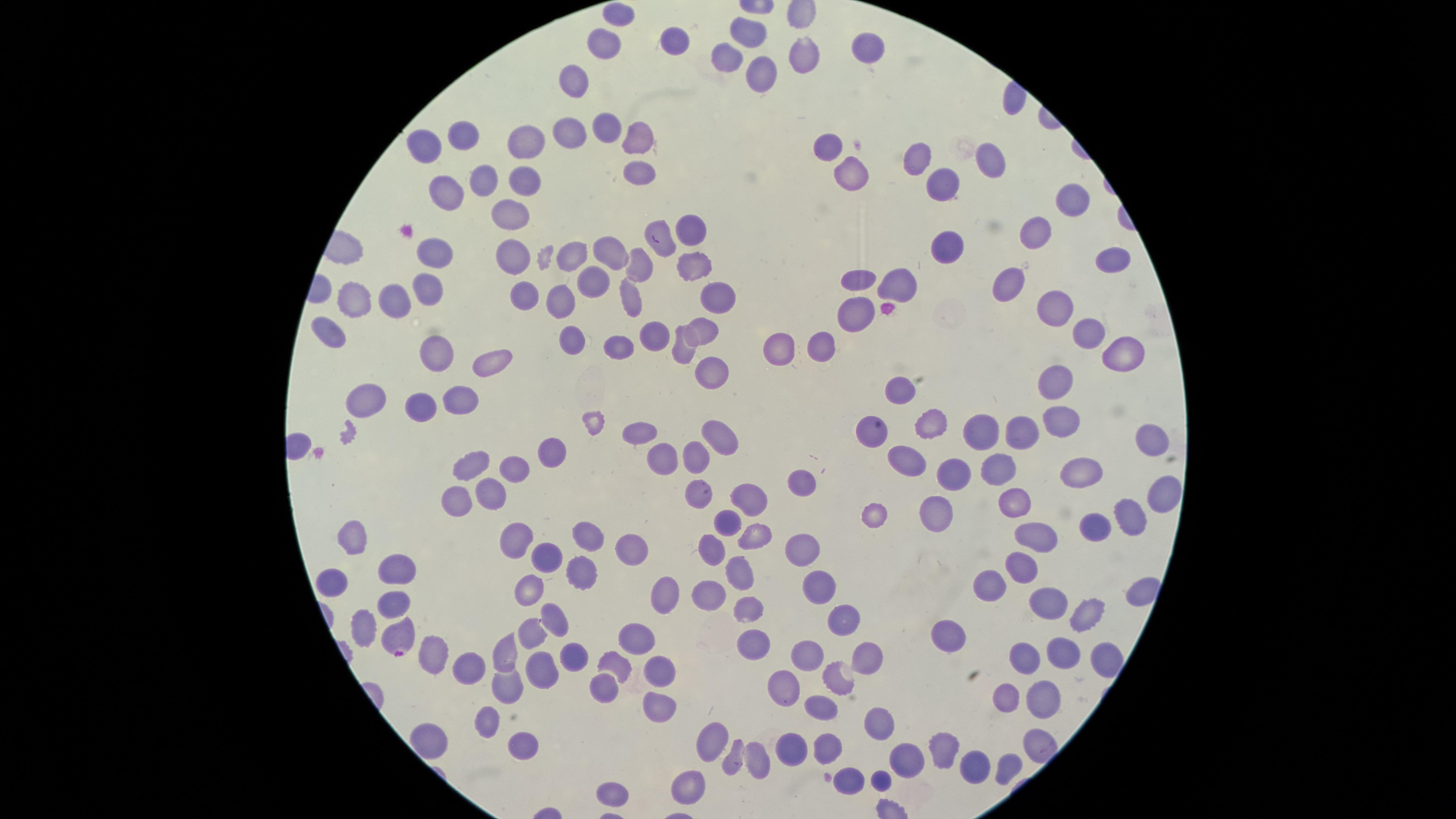

Approximate marker points as [x, y] in pixels.
Summary:
  - Parasitized red blood cells: [403, 639]
  - Uninfected red blood cells: [626, 18], [757, 31], [678, 38], [605, 46], [867, 46], [807, 52], [728, 60], [578, 75], [757, 83], [604, 126], [571, 132], [638, 134], [464, 138], [531, 138], [828, 144], [424, 153], [917, 157], [996, 165], [851, 171], [636, 173], [480, 180], [525, 185], [939, 190], [447, 194], [1076, 200], [510, 213], [690, 226], [659, 228], [1031, 236], [956, 247], [434, 253], [607, 254], [1111, 254], [517, 256], [574, 257], [689, 259], [640, 262], [1013, 279], [859, 280], [899, 284], [595, 286], [430, 288], [717, 291], [531, 294], [631, 298], [355, 299], [398, 299], [1056, 301], [563, 303], [854, 317], [701, 324], [654, 332], [1088, 334], [333, 337], [578, 339], [624, 341], [823, 342], [784, 349], [441, 350], [1119, 351], [679, 356], [487, 360], [714, 375], [1052, 385], [901, 389], [461, 400], [367, 402], [426, 410], [943, 424], [1061, 425], [647, 433], [1024, 433], [978, 434], [871, 436], [714, 441], [1152, 442], [546, 448], [908, 459], [664, 464], [694, 464], [1085, 465], [479, 467], [516, 469], [996, 473], [952, 478], [804, 479], [491, 491], [692, 491], [1160, 492], [758, 500], [457, 503], [1019, 503], [934, 512], [1133, 515], [876, 516], [732, 525], [1100, 526], [355, 534], [1046, 535], [593, 536], [757, 539], [517, 540], [631, 548], [802, 548], [719, 550], [545, 553], [1021, 563], [401, 568], [576, 574], [740, 576], [994, 583], [336, 585], [818, 586], [531, 591], [713, 596], [665, 598], [393, 600], [1043, 602], [746, 609], [555, 611], [847, 615], [1078, 618], [369, 626], [954, 629], [540, 635], [640, 641], [752, 643], [808, 649], [862, 650], [1057, 652], [572, 653], [436, 654], [1018, 655], [1105, 657], [507, 658], [544, 666], [615, 666], [662, 671], [465, 673], [840, 675], [781, 686], [604, 688], [508, 694], [1043, 696], [1007, 700], [818, 709], [661, 711], [882, 719], [491, 725], [436, 740], [711, 740], [526, 747], [824, 747], [947, 749], [790, 750], [733, 760], [758, 762], [977, 765], [1002, 765], [908, 766], [691, 782], [621, 792]
  - Capture: smartphone photograph through the microscope eyepiece
  - Species: Plasmodium falciparum
  - Visible region: circular
  - Field of view: single
  - Stain: Giemsa
  - Preparation: thin blood smear
  - Image size: 1456×819 pixels
  - Presence: malaria parasites seen